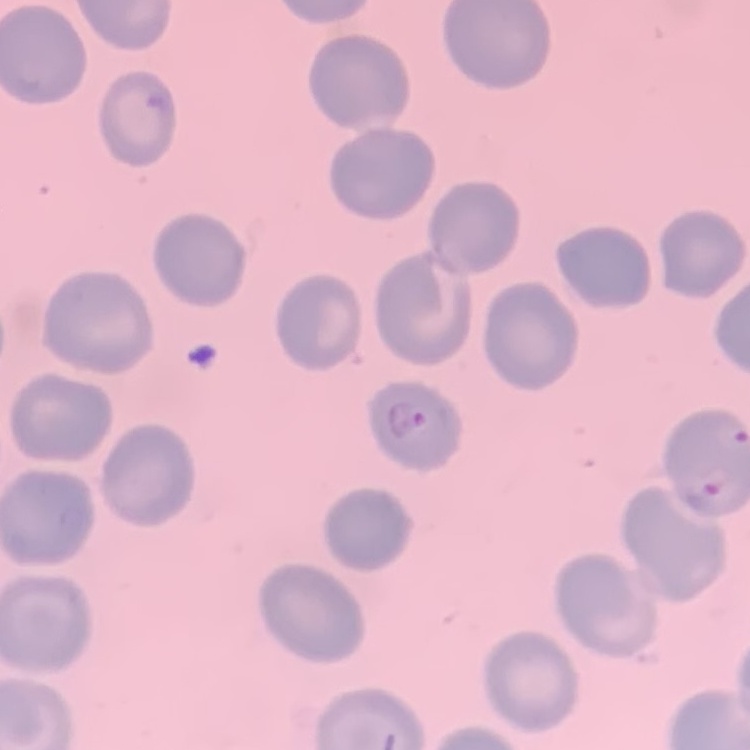

The red blood cells exhibit no rouleaux formation. Thin blood smear. Field's or Giemsa stain. One tile cut from a larger photomicrograph.